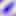

Photomicrograph. Toxoplasma gondii is seen. Captured at 400x magnification.